Assess this cell for malaria.
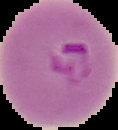

Parasitized.

From a thin blood film. Segmented cell region on a black background. Image is 118×130 pixels.